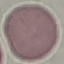
malaria status = uninfected
capture = smartphone through the microscope eyepiece
preparation = thin smear
image type = cell patch, automatically extracted from a larger field of view and resized to 64 × 64 pixels
stain = Giemsa